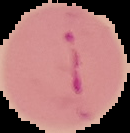
From a thin blood film. The area outside the segmented cell region is set to black. Malaria status: parasitized. Image is 130×133 pixels.